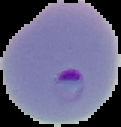 The area outside the segmented cell region is set to black. Image is 121×127 pixels. From a thin blood smear. Result: Plasmodium parasites identified.